Outline each blood parasite and name the species.
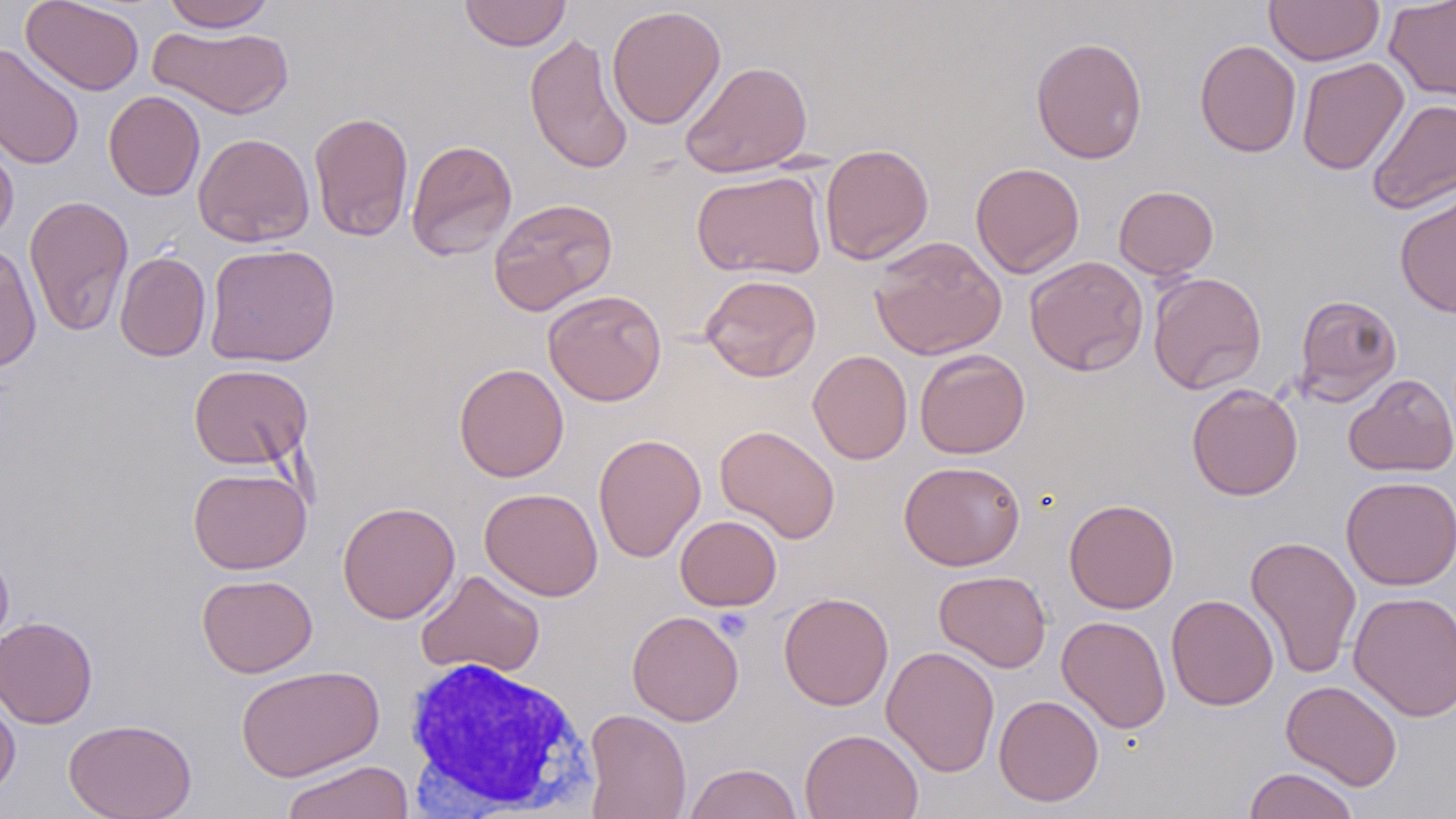

No blood parasites seen.

slide_level_diagnosis: negative for blood parasites
image_size: 1456×819 pixels
white_blood_cell_locations: 'approximate bounding boxes as [x1, y1, x2, y2] in pixels: [400, 655, 596, 816]'
preparation: thin blood film
modality: optical microscopy
field_of_view: one of a larger specimen
stain: May-Grünwald-Giemsa
uninfected_red_blood_cell_locations: 'approximate bounding boxes as [x1, y1, x2, y2] in pixels: [21, 0, 145, 95], [162, 0, 276, 32], [459, 0, 572, 51], [1264, 0, 1384, 66], [1384, 0, 1456, 102], [606, 5, 726, 130], [148, 25, 293, 118], [524, 32, 633, 175], [1030, 36, 1148, 164], [1194, 40, 1302, 158], [0, 42, 85, 171], [1296, 57, 1409, 175], [680, 60, 813, 178], [104, 90, 205, 200], [1366, 98, 1456, 215], [308, 111, 414, 242], [193, 133, 315, 247], [0, 135, 18, 247], [405, 139, 518, 261], [820, 143, 934, 265], [970, 161, 1085, 278], [692, 170, 828, 279], [1114, 185, 1219, 279], [1395, 191, 1456, 319], [24, 194, 134, 338], [488, 197, 617, 315], [869, 236, 1007, 361], [204, 243, 340, 367], [0, 244, 41, 373], [115, 251, 211, 361], [1025, 256, 1149, 376], [1148, 271, 1267, 394], [699, 274, 822, 382], [543, 289, 667, 406], [1293, 294, 1402, 405], [808, 349, 913, 465], [915, 349, 1030, 459], [453, 362, 569, 482], [188, 364, 313, 471], [1343, 374, 1456, 477], [1187, 383, 1303, 501], [715, 425, 840, 543], [593, 433, 706, 562], [899, 460, 1025, 570], [188, 467, 311, 574], [1341, 476, 1456, 590], [479, 487, 603, 601], [1064, 498, 1179, 614], [337, 501, 460, 624], [675, 515, 781, 611], [1245, 535, 1362, 680], [0, 542, 14, 652], [416, 569, 546, 678], [934, 570, 1052, 672], [197, 573, 318, 678], [1349, 590, 1455, 722], [778, 591, 894, 710], [1166, 594, 1278, 710], [627, 610, 744, 726], [1056, 615, 1171, 733], [0, 616, 97, 728], [881, 645, 1000, 777], [235, 664, 384, 782], [1281, 680, 1402, 791], [0, 691, 20, 801], [993, 694, 1104, 807], [584, 708, 692, 819], [63, 717, 197, 819], [799, 728, 924, 819], [280, 759, 415, 819], [684, 763, 803, 819], [1243, 767, 1360, 819]'
magnification: 1000x